Locate and identify every blood parasite.
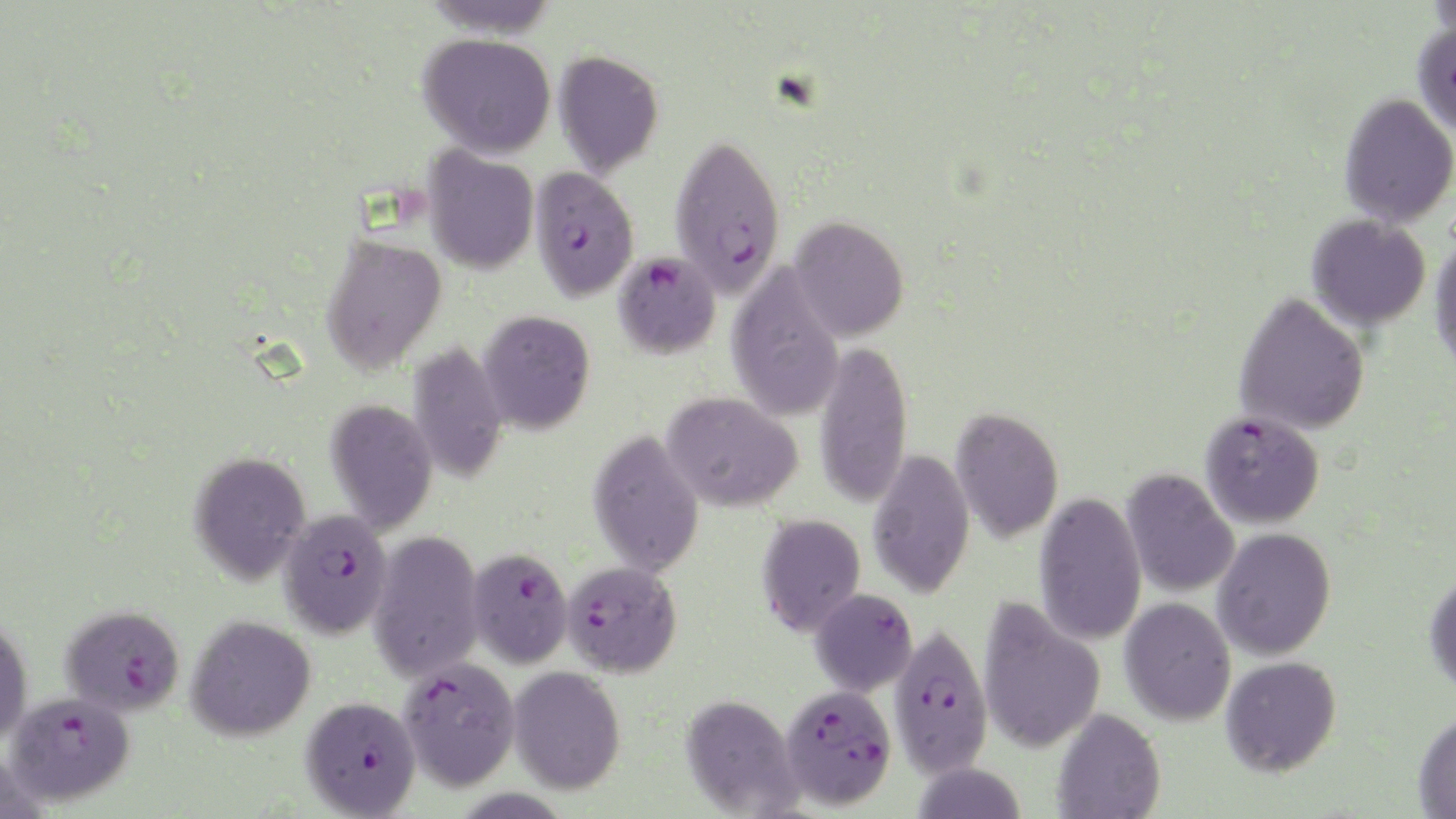

Approximate bounding boxes as (x1, y1, x2, y2) in pixels.
Plasmodium falciparum-infected red blood cells: (1411, 19, 1456, 136), (669, 132, 786, 297), (529, 166, 639, 302), (614, 251, 721, 359), (1199, 410, 1324, 529), (278, 509, 393, 639), (467, 547, 573, 668), (561, 560, 682, 677), (60, 604, 185, 716), (888, 621, 993, 778), (397, 656, 520, 791), (780, 682, 897, 810), (5, 690, 135, 805), (300, 695, 421, 817).
No Plasmodium ovale, Plasmodium malariae, Plasmodium vivax, Babesia divergens, or Trypanosoma brucei observed.

slide-level diagnosis = Plasmodium falciparum
preparation = thin blood smear
stain = May-Grünwald-Giemsa
uninfected red blood cell locations = approximate bounding boxes as (x1, y1, x2, y2) in pixels: (420, 0, 559, 38), (418, 32, 556, 158), (553, 50, 664, 178), (1338, 93, 1456, 227), (422, 146, 539, 275), (1306, 213, 1431, 330), (788, 216, 909, 342), (1429, 233, 1456, 377), (320, 234, 447, 375), (726, 265, 845, 420), (1233, 291, 1370, 436), (478, 310, 595, 434), (814, 340, 913, 509), (407, 342, 510, 486), (661, 392, 802, 512), (325, 398, 437, 535), (950, 407, 1064, 544), (587, 429, 704, 577), (867, 449, 975, 598), (189, 450, 311, 585), (1121, 468, 1239, 598), (1033, 491, 1147, 645), (756, 513, 866, 637), (1212, 527, 1336, 661), (368, 529, 484, 682), (1424, 571, 1456, 699), (810, 588, 917, 695), (1120, 597, 1236, 725), (977, 598, 1106, 754), (186, 615, 316, 741), (0, 616, 33, 746), (1221, 656, 1342, 777), (508, 666, 625, 795), (680, 693, 802, 817), (1051, 708, 1166, 819), (1412, 710, 1456, 819), (909, 761, 1028, 818)
image size = 1456×819 pixels
field of view = one of a larger specimen
magnification = 1000x
modality = light microscopy